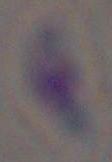
identification = Toxoplasma gondii
magnification = 1000x
modality = photomicrograph